Assess this cell for malaria.
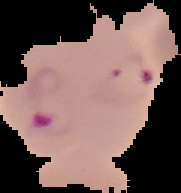

It is parasitized.

Summary:
  - Preparation: thin blood smear
  - Image type: cell region segmented out of the field of view; surrounding area masked to black
  - Image size: 181×193 pixels